Find each white blood cell.
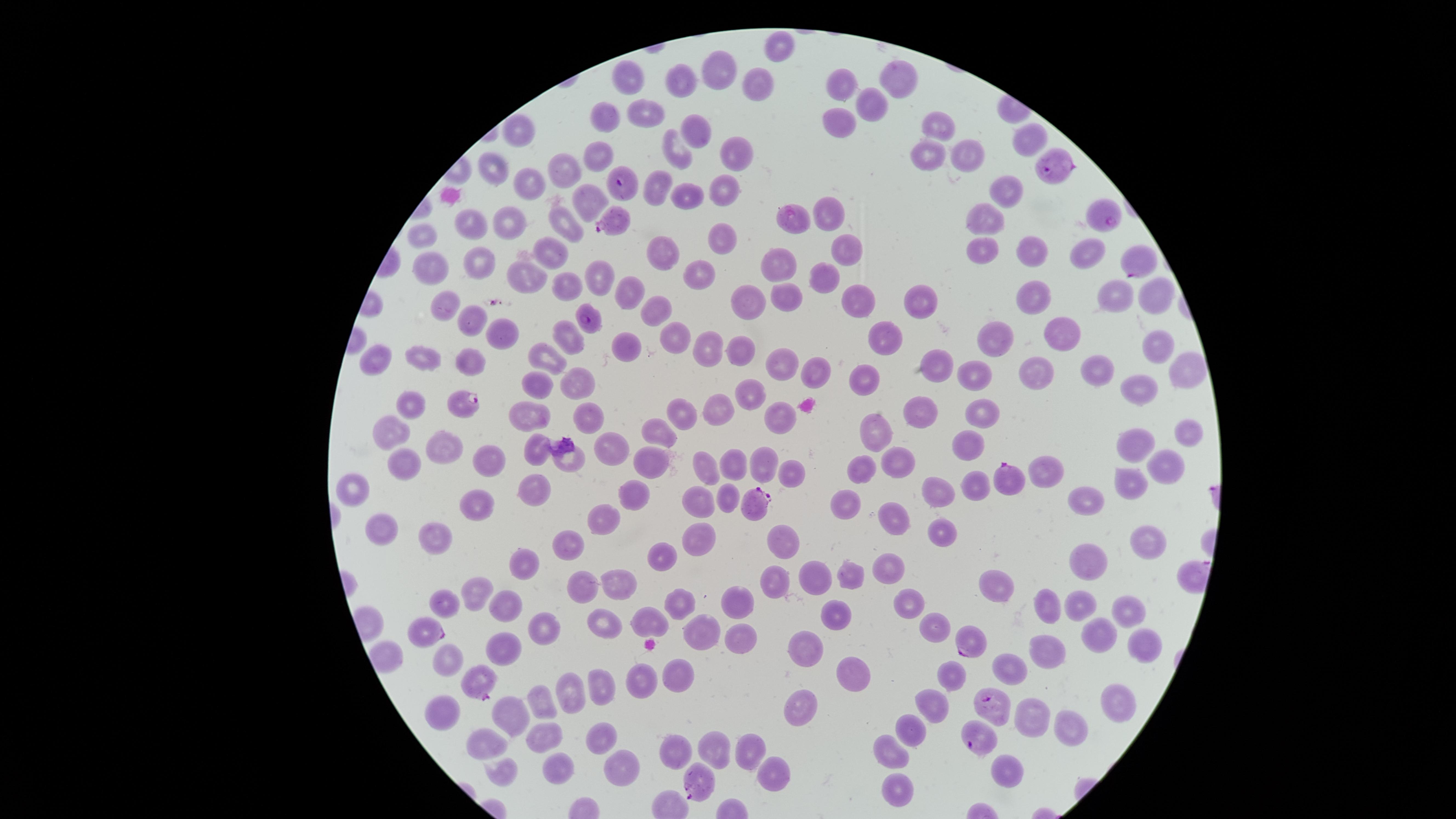
No white blood cells identified.

Approximate marker points, in pixels from the top-left corner. Parasitized red blood cells: (x=1050, y=164), (x=618, y=182), (x=1104, y=215), (x=612, y=222), (x=1139, y=260), (x=587, y=318), (x=460, y=406), (x=1007, y=479), (x=748, y=505), (x=424, y=632), (x=969, y=640), (x=477, y=680), (x=990, y=709), (x=976, y=737), (x=701, y=782). Uninfected red blood cells: (x=717, y=74), (x=633, y=77), (x=895, y=79), (x=835, y=85), (x=757, y=87), (x=681, y=88), (x=875, y=105), (x=611, y=114), (x=649, y=115), (x=838, y=120), (x=936, y=123), (x=695, y=133), (x=1029, y=138), (x=520, y=140), (x=927, y=152), (x=678, y=154), (x=734, y=154), (x=599, y=155), (x=962, y=155), (x=566, y=169), (x=488, y=176), (x=658, y=186), (x=722, y=190), (x=1004, y=190), (x=530, y=193), (x=686, y=195), (x=585, y=202), (x=830, y=212), (x=511, y=220), (x=987, y=220), (x=472, y=223), (x=797, y=223), (x=565, y=225), (x=421, y=235), (x=722, y=236), (x=982, y=242), (x=844, y=246), (x=547, y=251), (x=1025, y=251), (x=1081, y=251), (x=661, y=252), (x=475, y=262), (x=429, y=263), (x=780, y=265), (x=528, y=275), (x=697, y=276), (x=601, y=277), (x=819, y=279), (x=561, y=285), (x=1152, y=289), (x=628, y=292), (x=857, y=294), (x=1114, y=297), (x=786, y=298), (x=917, y=298), (x=749, y=303), (x=1040, y=303), (x=442, y=304), (x=657, y=308), (x=468, y=323), (x=494, y=332), (x=1056, y=332), (x=670, y=334), (x=884, y=337), (x=570, y=338), (x=995, y=339), (x=710, y=344), (x=627, y=347), (x=1153, y=349), (x=740, y=354), (x=424, y=357), (x=546, y=357), (x=466, y=358), (x=378, y=362), (x=784, y=362), (x=936, y=368), (x=1183, y=370), (x=811, y=371), (x=1097, y=372), (x=973, y=373), (x=1032, y=373), (x=865, y=378), (x=542, y=383), (x=580, y=384), (x=1135, y=390), (x=750, y=393), (x=412, y=403), (x=718, y=406), (x=922, y=411), (x=533, y=413), (x=588, y=413), (x=680, y=415), (x=983, y=415), (x=781, y=418), (x=396, y=431), (x=875, y=433), (x=1186, y=433), (x=661, y=437), (x=608, y=442), (x=439, y=444), (x=1136, y=444), (x=537, y=445), (x=970, y=451), (x=572, y=455), (x=486, y=458), (x=764, y=461), (x=407, y=462), (x=736, y=462), (x=896, y=462), (x=1164, y=463), (x=650, y=466), (x=702, y=467), (x=862, y=470), (x=789, y=471), (x=1048, y=471), (x=1129, y=482), (x=353, y=485), (x=536, y=486), (x=977, y=488), (x=640, y=490), (x=939, y=490), (x=724, y=496), (x=1083, y=497), (x=847, y=498), (x=479, y=502), (x=698, y=502), (x=893, y=513), (x=607, y=521), (x=377, y=528), (x=941, y=530), (x=701, y=534), (x=436, y=537), (x=1148, y=540), (x=786, y=545), (x=568, y=546), (x=664, y=555), (x=1088, y=562), (x=885, y=564), (x=850, y=570), (x=522, y=571), (x=820, y=573), (x=618, y=580), (x=773, y=581), (x=1001, y=583), (x=477, y=588), (x=584, y=592), (x=682, y=598), (x=739, y=598), (x=907, y=601), (x=500, y=604), (x=1049, y=606), (x=1079, y=608), (x=1132, y=611), (x=834, y=615), (x=649, y=622), (x=542, y=625), (x=934, y=626), (x=600, y=628), (x=1096, y=631), (x=700, y=632), (x=737, y=638), (x=809, y=643), (x=1144, y=643), (x=501, y=647), (x=1043, y=648), (x=386, y=655), (x=445, y=659), (x=852, y=667), (x=1007, y=668), (x=954, y=675), (x=636, y=678), (x=675, y=680), (x=599, y=685), (x=574, y=695), (x=1108, y=696), (x=802, y=699), (x=935, y=707), (x=543, y=708), (x=443, y=711), (x=514, y=713), (x=1030, y=721), (x=1064, y=726), (x=912, y=727), (x=599, y=735), (x=544, y=737), (x=483, y=746), (x=708, y=748), (x=753, y=751), (x=889, y=753), (x=679, y=754), (x=556, y=767), (x=1009, y=769), (x=622, y=771), (x=505, y=773), (x=771, y=778), (x=892, y=781). Giemsa stain. Species: Plasmodium falciparum. Image is 1456×819 pixels. Thin smear of blood. Single field of view. Presence: malaria parasites identified. Circular visible region. Smartphone photograph through the microscope eyepiece.